Locate every Plasmodium falciparum-infected red blood cell.
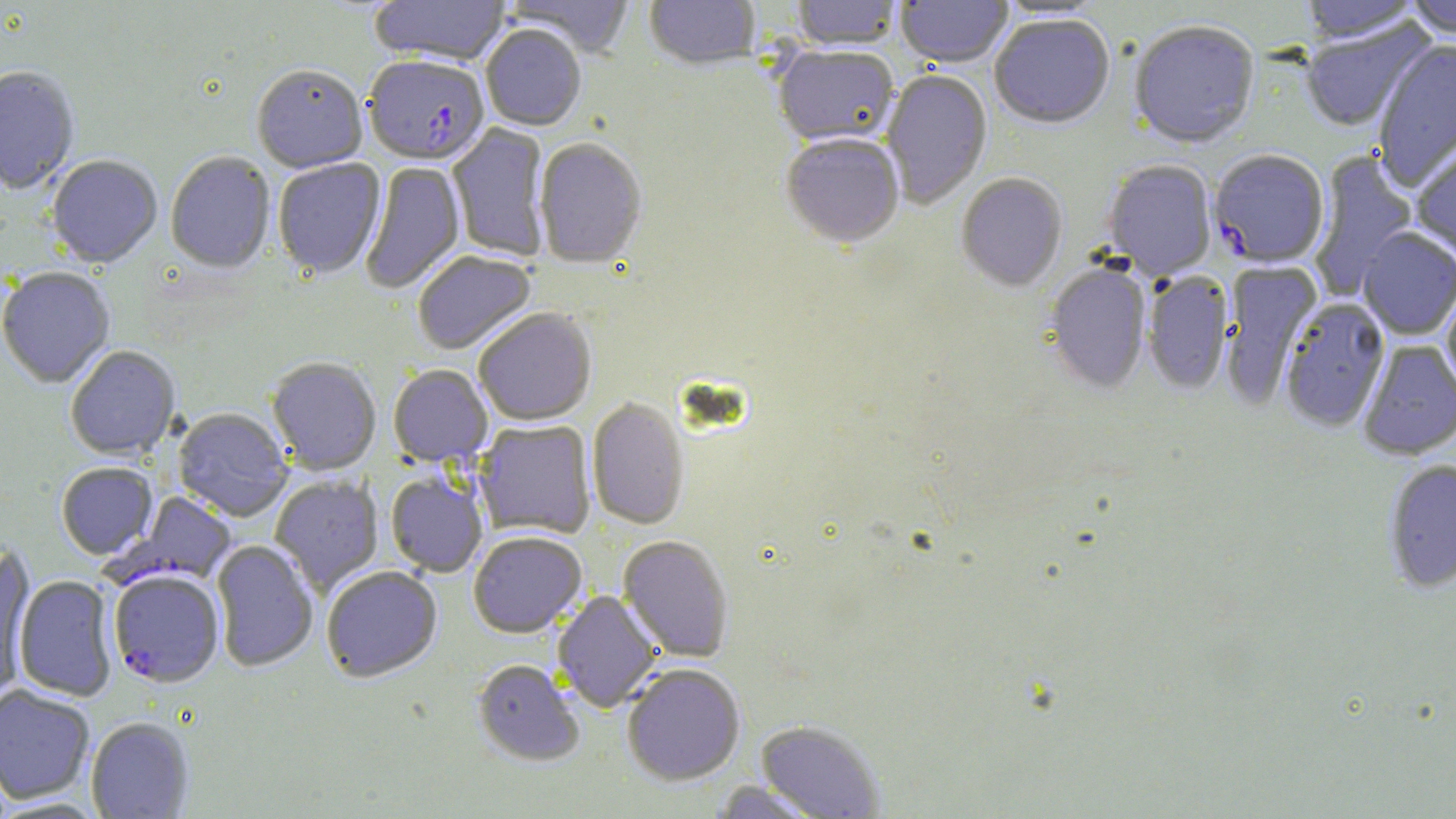

Approximate bounding boxes as (x1,y1)-(x2,y2) corner pairs in pixels.
Plasmodium falciparum-infected red blood cells: (363,58)-(489,167), (1209,151)-(1329,270), (110,491)-(238,589), (109,570)-(224,689).

slide_level_diagnosis: Plasmodium falciparum
image_size: 1456×819 pixels
modality: optical microscopy
preparation: thin blood film
stain: May-Grünwald-Giemsa
field_of_view: single
magnification: 1000x
uninfected_red_blood_cell_locations: 'approximate bounding boxes as (x1,y1)-(x2,y2) corner pairs in pixels: (369,0)-(511,68), (505,0)-(635,60), (645,0)-(760,73), (790,0)-(902,52), (895,0)-(1013,70), (1298,0)-(1423,45), (1405,0)-(1456,41), (992,1)-(1110,21), (990,17)-(1115,131), (1299,20)-(1433,134), (1129,22)-(1260,151), (480,27)-(586,132), (1373,42)-(1456,190), (774,48)-(899,148), (0,68)-(80,196), (251,68)-(367,175), (881,70)-(992,210), (447,124)-(550,262), (780,135)-(904,250), (534,139)-(648,271), (1412,139)-(1456,262), (1308,150)-(1419,302), (165,152)-(276,276), (46,157)-(163,270), (273,159)-(386,281), (1103,161)-(1216,281), (359,162)-(466,294), (956,174)-(1068,294), (1357,229)-(1456,340), (413,252)-(537,356), (1221,262)-(1323,408), (1044,264)-(1152,394), (0,268)-(116,389), (1143,272)-(1233,395), (1442,286)-(1456,398), (1280,299)-(1391,433), (474,310)-(596,427), (1359,341)-(1456,461), (65,346)-(181,461), (267,358)-(381,475), (388,365)-(493,467), (587,399)-(690,530), (173,408)-(293,523), (474,420)-(596,539), (1384,460)-(1456,594), (56,463)-(158,560), (386,472)-(488,578), (269,474)-(384,595), (468,532)-(587,639), (618,536)-(734,662), (211,540)-(318,673), (1,547)-(35,698), (321,567)-(442,684), (13,575)-(118,702), (552,589)-(663,713), (472,659)-(584,768), (622,665)-(745,786), (0,685)-(95,805), (86,717)-(194,818), (755,721)-(884,818), (711,781)-(827,818)'